Name the cell type shown.
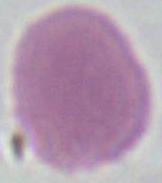
An erythrocyte.

Summary:
  - Modality: micrograph
  - Magnification: 1000x